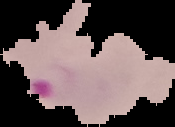
Malaria status: parasitized. Segmented cell region on a black background. From a thin blood smear. Image is 175×127 pixels.